Outline each blood parasite and name the species.
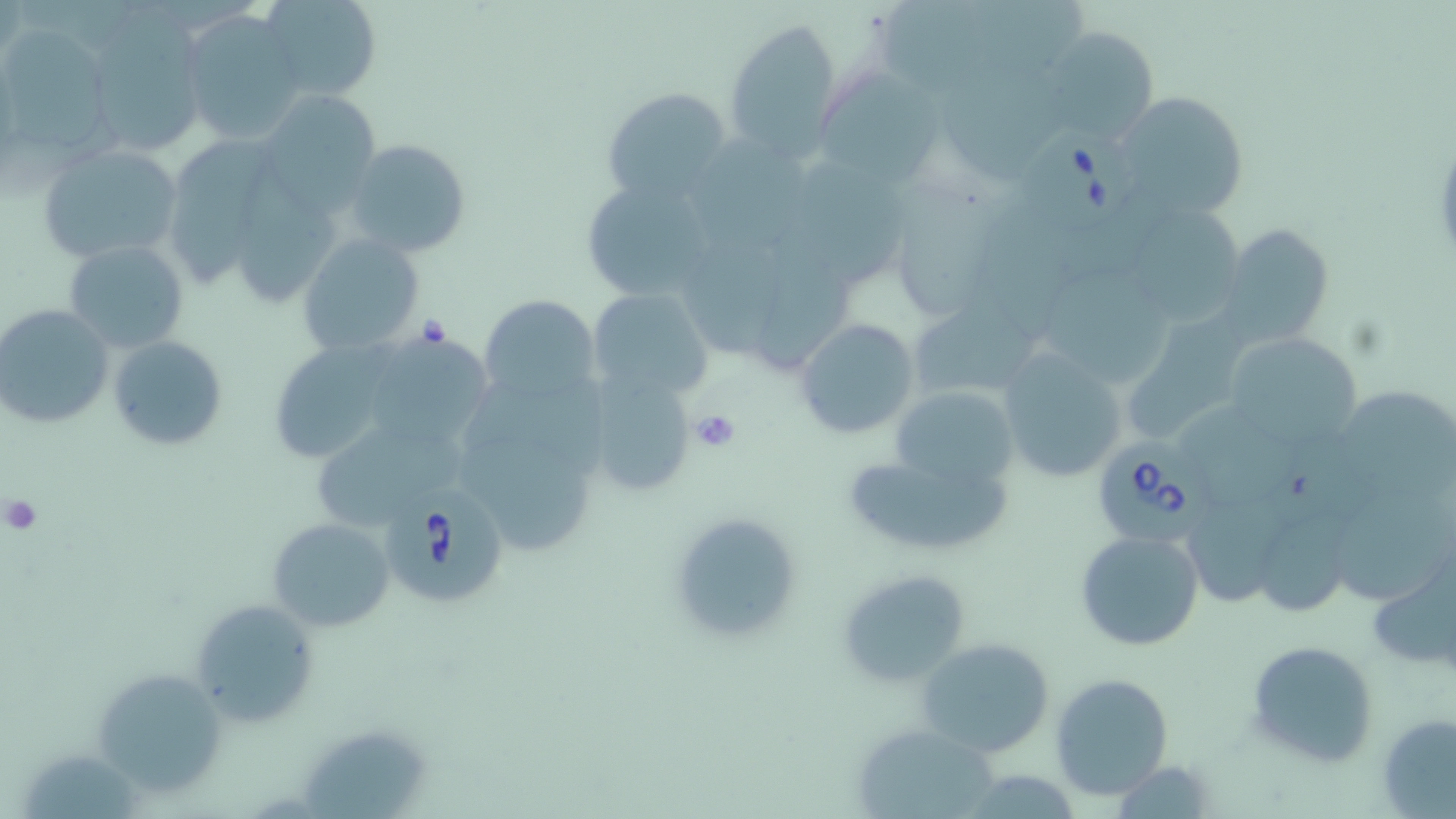

Approximate bounding boxes as (x1, y1, x2, y2) in pixels.
Babesia divergens-infected red blood cells: (1015, 121, 1146, 237), (1091, 439, 1206, 548), (381, 487, 514, 609).
No Plasmodium falciparum, Plasmodium ovale, Plasmodium malariae, Plasmodium vivax, or Trypanosoma brucei observed.

Platelet locations: (416, 315, 450, 350), (689, 408, 742, 453), (2, 493, 43, 537). Uninfected red blood cell locations: (258, 0, 382, 101), (176, 11, 304, 142), (724, 17, 843, 158), (80, 26, 208, 159), (1042, 27, 1159, 147), (1, 32, 114, 154), (943, 52, 1076, 179), (826, 63, 950, 189), (601, 86, 733, 204), (1109, 89, 1253, 225), (259, 91, 382, 208), (692, 131, 814, 248), (172, 137, 270, 294), (343, 138, 474, 259), (37, 141, 186, 265), (239, 160, 341, 307), (803, 165, 914, 291), (578, 176, 719, 302), (880, 188, 1008, 322), (1125, 208, 1246, 323), (1221, 225, 1336, 348), (762, 226, 858, 366), (297, 234, 426, 358), (64, 238, 188, 352), (686, 241, 786, 358), (1044, 266, 1180, 391), (588, 287, 712, 402), (478, 294, 599, 404), (906, 298, 1042, 402), (0, 304, 114, 429), (1120, 310, 1252, 444), (794, 318, 921, 440), (1221, 331, 1360, 452), (274, 333, 394, 461), (108, 334, 229, 452), (365, 334, 496, 444), (994, 348, 1130, 484), (582, 374, 697, 495), (890, 384, 1020, 492), (1340, 387, 1456, 496), (1173, 400, 1297, 504), (317, 416, 469, 530), (463, 429, 599, 554), (855, 454, 1015, 551), (1337, 487, 1456, 600), (1243, 493, 1366, 625), (1188, 497, 1298, 608), (667, 510, 808, 645), (266, 517, 396, 633), (1075, 529, 1206, 651), (1363, 548, 1455, 674), (836, 568, 972, 687), (188, 598, 323, 728), (915, 636, 1055, 758), (1245, 638, 1381, 767), (88, 667, 231, 797), (1050, 673, 1175, 801), (1377, 711, 1456, 817), (858, 726, 1002, 819), (301, 731, 428, 819), (1108, 761, 1221, 817), (969, 772, 1071, 819). Slide-level diagnosis: Babesia divergens. Image is 1456×819 pixels. Thin blood smear. Single field of view. Optical microscopy. Captured at 1000x magnification. May-Grünwald-Giemsa stain.